Report the malaria status of this cell.
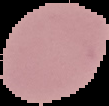
Uninfected.

Summary:
  - Image size: 109×106 pixels
  - Image type: cell region segmented out of the field of view; surrounding area masked to black
  - Preparation: thin blood film